Assess this cell for malaria.
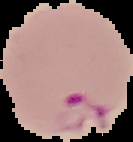
It is parasitized.

Image is 133×142 pixels. Segmented cell region on a black background. From a thin blood smear.